Outline each blood parasite and name the species.
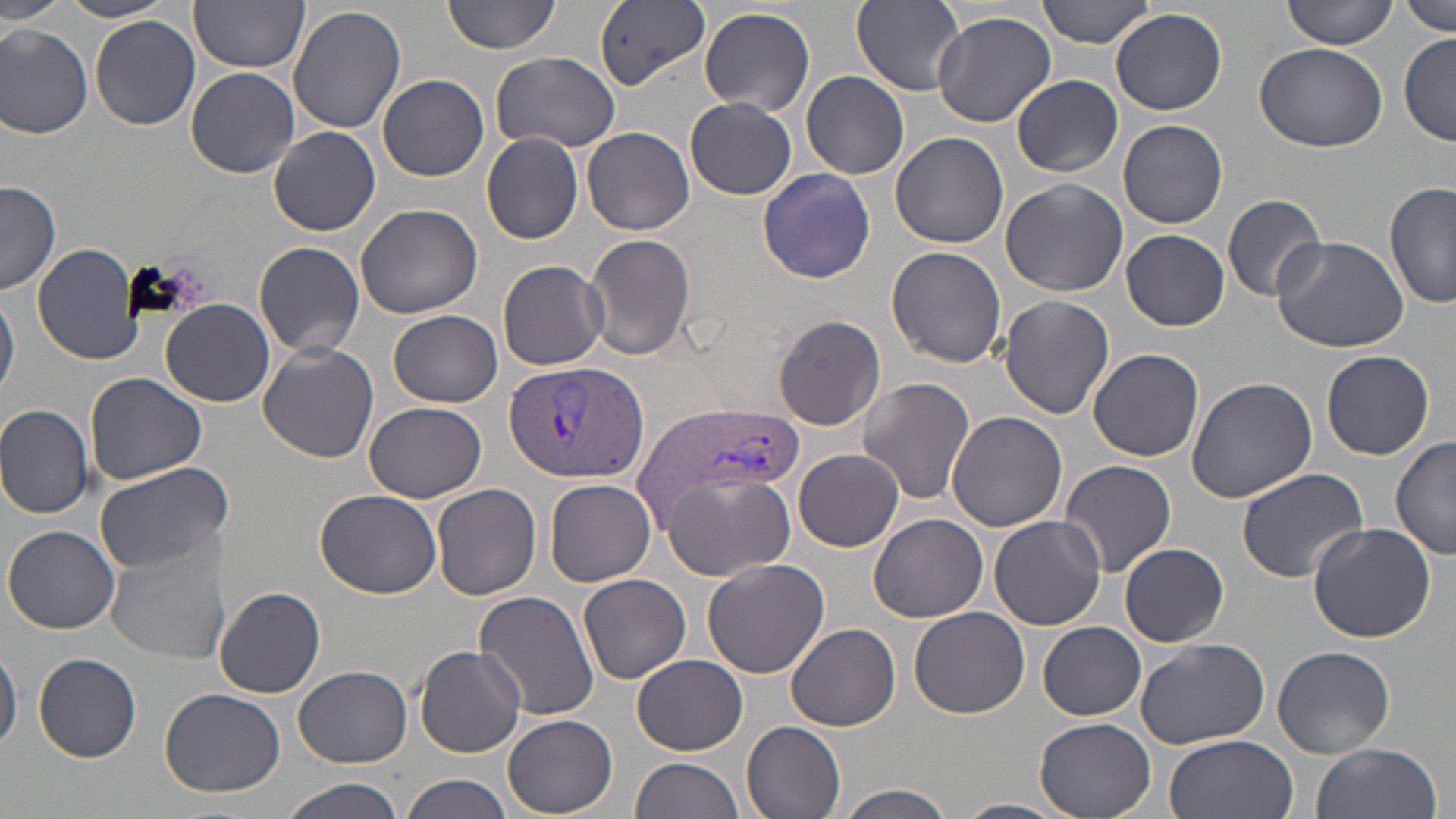
Approximate bounding boxes as (x1, y1, x2, y2) in pixels.
Plasmodium vivax-infected red blood cells: (504, 357, 650, 486), (638, 403, 801, 520).
No Plasmodium falciparum, Plasmodium ovale, Plasmodium malariae, Babesia divergens, or Trypanosoma brucei observed.

Uninfected red blood cell locations: (1, 0, 68, 24), (60, 0, 180, 22), (444, 0, 561, 54), (1038, 0, 1161, 48), (1284, 0, 1399, 51), (190, 1, 308, 73), (852, 1, 967, 97), (1401, 1, 1454, 35), (593, 2, 712, 94), (291, 4, 407, 135), (698, 6, 816, 116), (1111, 7, 1228, 116), (931, 11, 1058, 129), (89, 15, 202, 131), (0, 26, 93, 138), (1400, 34, 1455, 146), (1254, 41, 1391, 150), (491, 52, 623, 155), (186, 67, 299, 178), (800, 71, 910, 179), (379, 74, 489, 181), (1012, 75, 1123, 177), (685, 99, 797, 199), (1119, 119, 1227, 230), (269, 126, 380, 236), (583, 127, 696, 236), (482, 132, 584, 244), (890, 132, 1008, 249), (757, 167, 875, 283), (999, 179, 1127, 296), (0, 180, 60, 295), (1385, 181, 1455, 311), (1222, 192, 1328, 302), (355, 204, 482, 318), (1121, 229, 1231, 331), (583, 234, 695, 362), (1268, 234, 1410, 353), (254, 241, 365, 356), (31, 242, 145, 365), (886, 245, 1007, 367), (498, 259, 609, 370), (0, 292, 20, 399), (998, 296, 1115, 420), (161, 299, 275, 406), (389, 311, 503, 407), (771, 315, 885, 429), (258, 342, 379, 463), (1088, 348, 1205, 461), (1321, 349, 1434, 460), (85, 373, 207, 485), (1185, 376, 1317, 504), (858, 377, 975, 506), (366, 401, 486, 502), (0, 403, 93, 520), (948, 411, 1067, 532), (1392, 433, 1455, 559), (794, 449, 905, 553), (1058, 459, 1178, 578), (94, 462, 232, 576), (1234, 467, 1372, 585), (664, 472, 795, 580), (544, 477, 657, 586), (432, 482, 541, 602), (314, 489, 441, 600), (869, 514, 988, 622), (989, 516, 1105, 630), (1307, 522, 1436, 644), (5, 526, 120, 634), (105, 537, 230, 666), (1120, 543, 1229, 645), (703, 559, 829, 679), (578, 574, 692, 683), (215, 586, 326, 697), (474, 590, 600, 721), (909, 608, 1029, 719), (1038, 621, 1147, 719), (787, 623, 901, 731), (1134, 637, 1270, 749), (414, 644, 526, 758), (1273, 645, 1396, 757), (0, 647, 21, 754), (32, 651, 142, 762), (632, 655, 748, 755), (293, 664, 413, 766), (160, 688, 286, 798), (502, 713, 618, 818), (1034, 718, 1156, 819), (742, 719, 847, 819), (1165, 733, 1298, 819), (1310, 742, 1443, 819), (631, 757, 743, 819), (400, 772, 513, 819), (279, 776, 407, 819), (834, 784, 957, 819), (952, 799, 1070, 819). Slide-level diagnosis: Plasmodium vivax. Image is 1456×819 pixels. Thin blood film. May-Grünwald-Giemsa-stained preparation. Light microscopy. Captured at 1000x magnification. Single field of view.